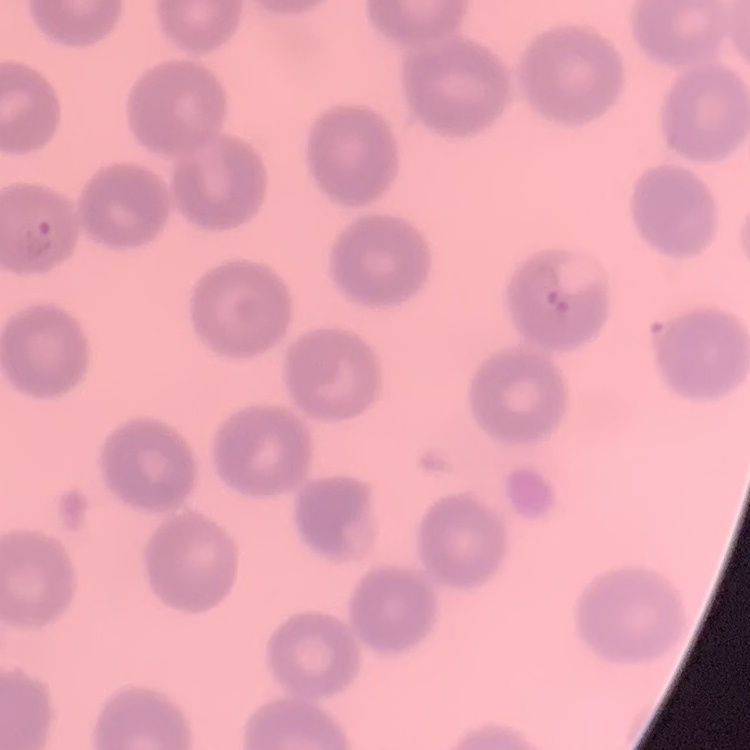
Summary:
  - Red blood cell morphology: no rouleaux formation
  - Stain: Field's or Giemsa
  - Preparation: thin blood film
  - Image type: one tile cut from a larger photomicrograph